Identify the blood parasite species.
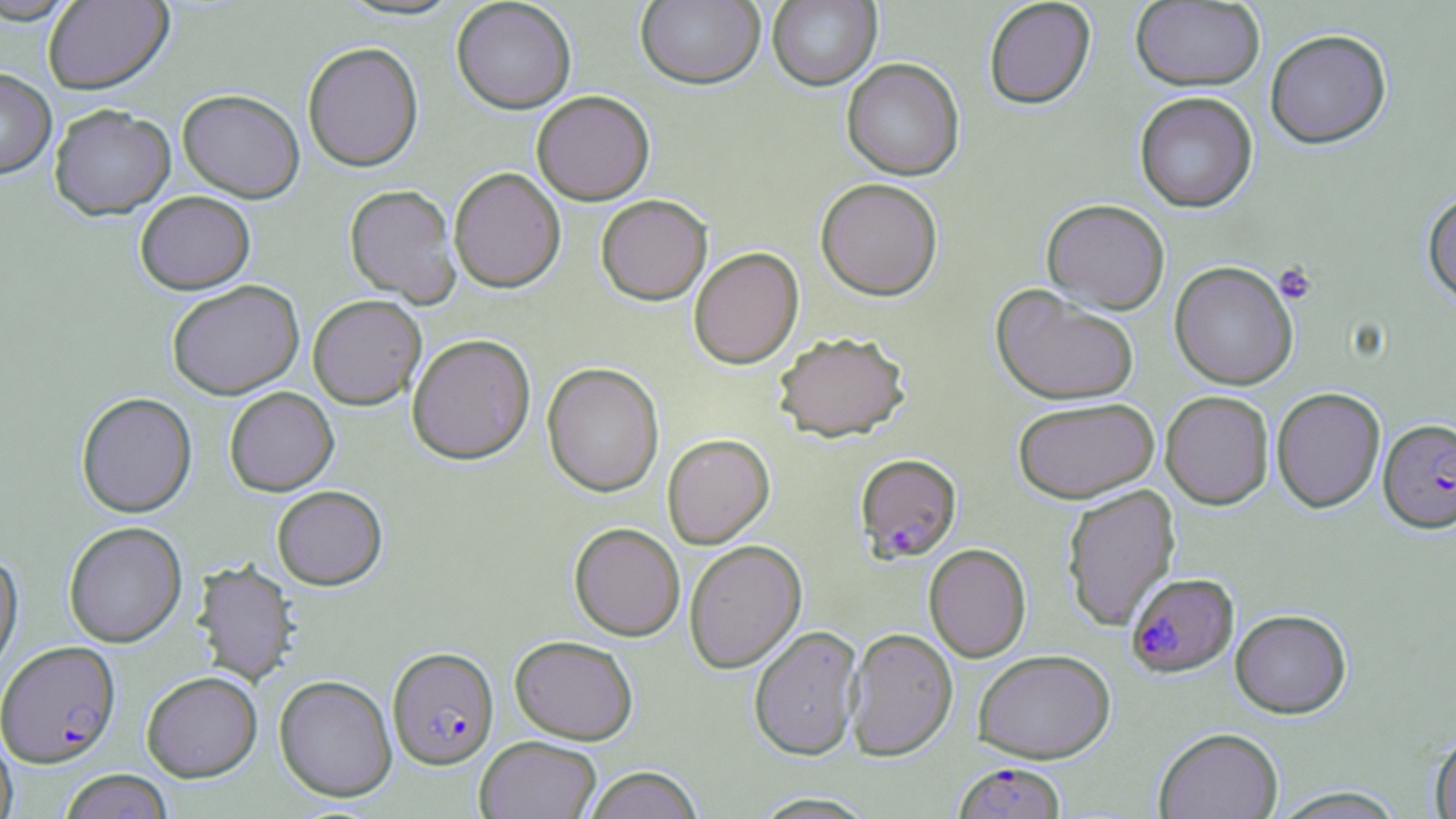
Plasmodium falciparum.

Approximate bounding boxes as (x1,y1)-(x2,y2) corner pairs in pixels. Platelet locations: (1273,262)-(1318,304). Uninfected red blood cell locations: (0,0)-(81,24), (43,0)-(173,94), (451,0)-(576,113), (635,0)-(765,89), (767,0)-(882,90), (983,0)-(1096,109), (1131,1)-(1265,91), (1265,28)-(1391,148), (302,41)-(424,172), (841,58)-(965,181), (0,68)-(56,179), (177,89)-(305,202), (532,91)-(655,205), (1134,91)-(1258,213), (49,104)-(175,220), (449,167)-(565,293), (815,177)-(943,300), (344,184)-(461,307), (1422,190)-(1456,308), (135,191)-(255,294), (596,194)-(712,305), (1041,199)-(1170,314), (688,247)-(804,369), (1169,261)-(1298,389), (167,280)-(304,399), (990,284)-(1140,405), (308,294)-(426,410), (772,331)-(911,443), (407,333)-(535,465), (542,363)-(664,498), (225,386)-(338,495), (1271,386)-(1385,513), (1160,390)-(1274,509), (76,392)-(197,517), (1013,397)-(1159,503), (662,433)-(775,549), (1061,483)-(1180,631), (272,485)-(388,590), (63,521)-(187,647), (569,523)-(685,641), (570,531)-(806,647), (684,540)-(806,674), (924,543)-(1031,662), (0,552)-(23,674), (192,560)-(297,686), (1230,608)-(1351,718), (748,625)-(863,761), (845,628)-(957,760), (509,635)-(638,744), (973,649)-(1115,763), (141,671)-(262,782), (274,675)-(397,802), (0,727)-(17,819), (1154,727)-(1284,819), (1428,729)-(1456,819), (475,736)-(601,819), (583,766)-(704,819), (58,769)-(173,819), (1269,786)-(1408,818), (749,792)-(881,818). Plasmodium falciparum-infected red blood cell locations: (1379,418)-(1456,533), (855,453)-(962,562), (1126,572)-(1238,677), (1,641)-(120,767), (387,647)-(499,769), (953,762)-(1066,819). 1000x magnification. Light microscopy. One field of a larger specimen. Thin blood film. Image is 1456×819 pixels. May-Grünwald-Giemsa stain.